Describe the morphology of the red blood cells.
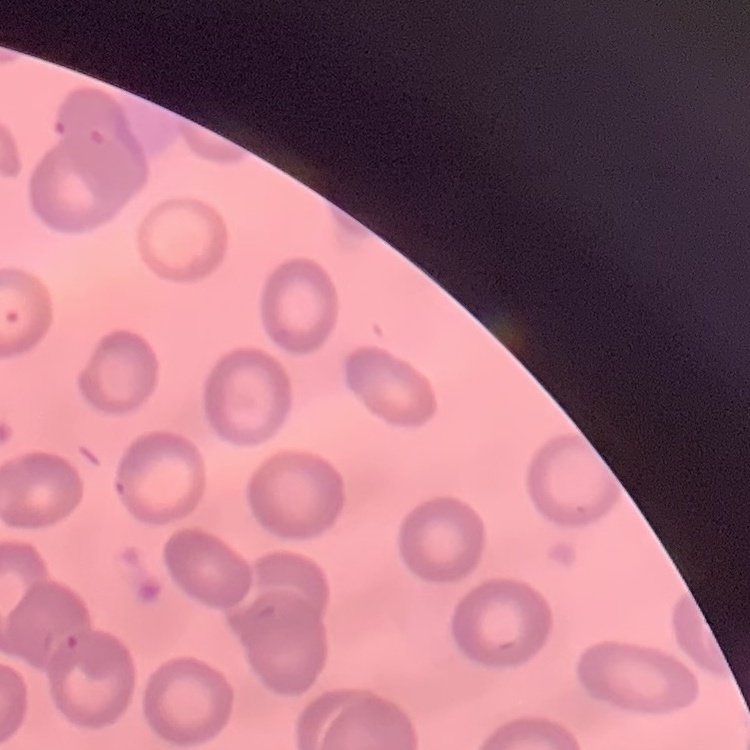

They show no rouleaux formation.

Summary:
  - Preparation: thin blood smear
  - Image type: square crop of a larger photomicrograph
  - Stain: Field's or Giemsa